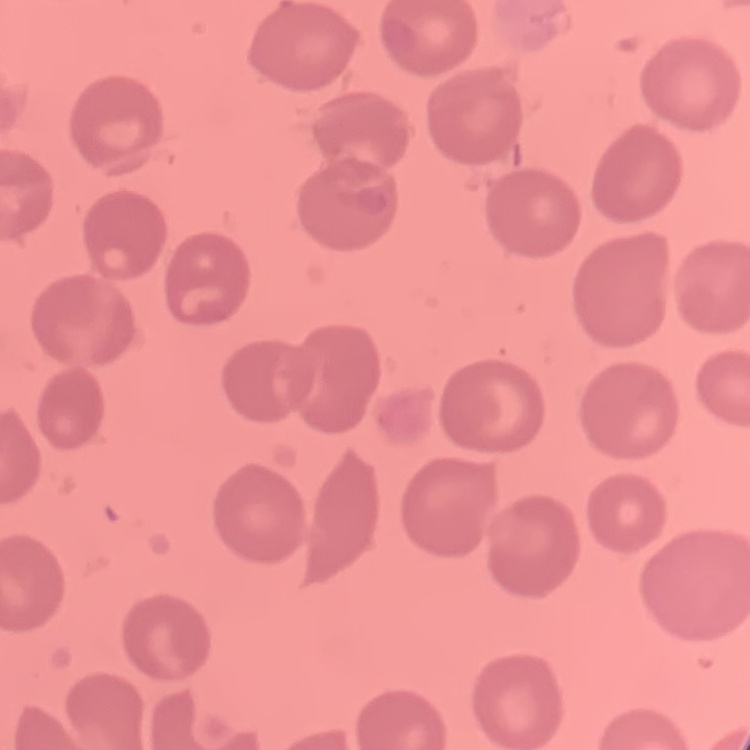 The red blood cells exhibit no rouleaux formation. Field's or Giemsa stain. Thin blood smear. One tile cut from a larger photomicrograph.